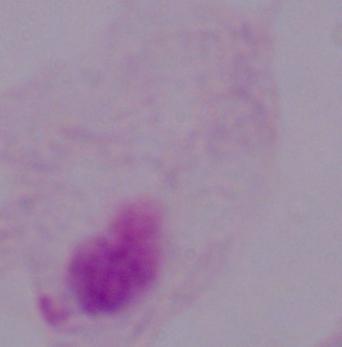

{
  "modality": "photomicrograph",
  "identification": "trichomonad",
  "magnification": "1000x"
}